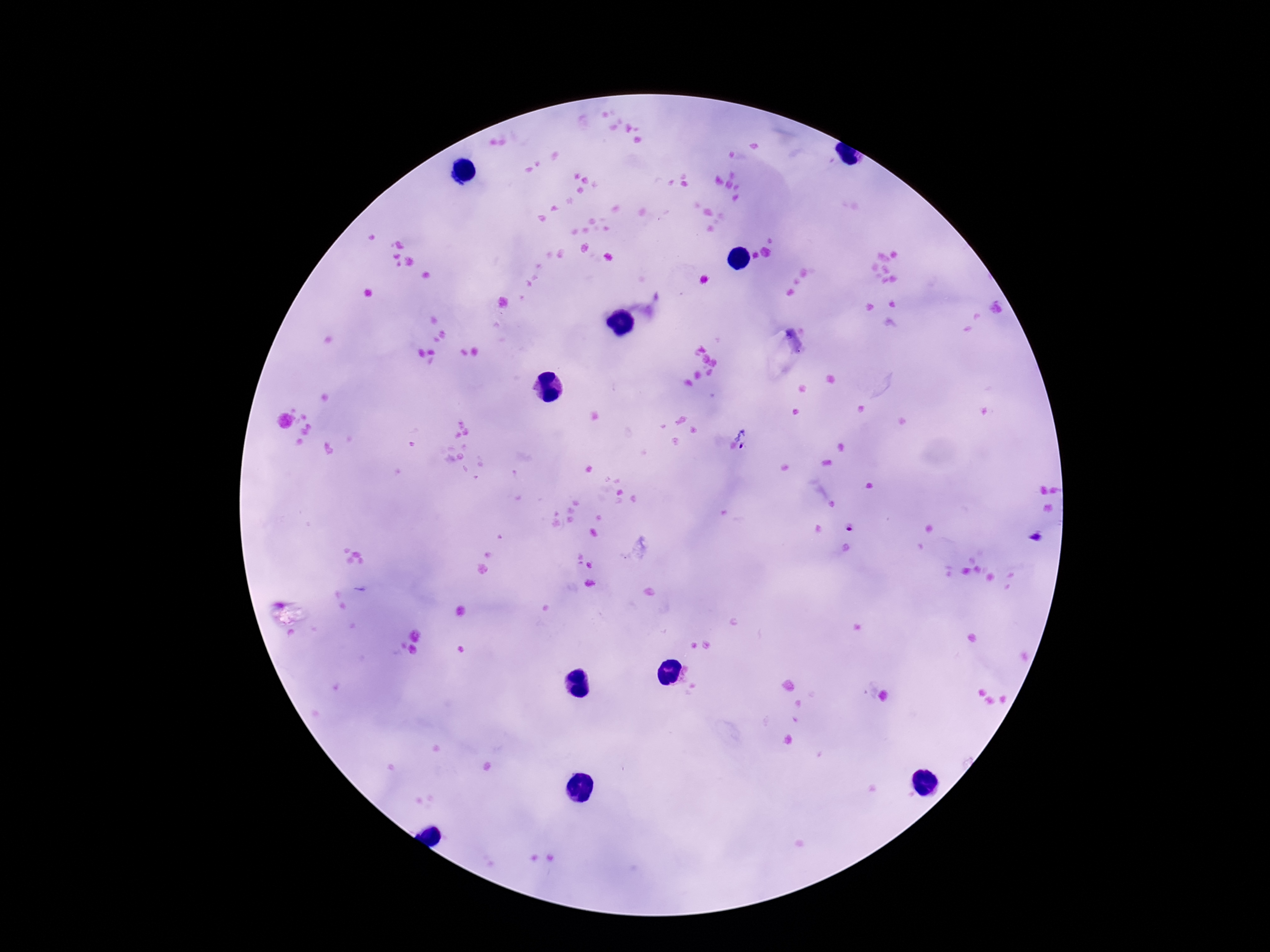

field_of_view: single
capture: smartphone camera through the microscope eyepiece
plasmodium_parasite_locations: 'approximate centers as (x, y) in pixels: (747, 438), (850, 529), (1036, 537)'
stain: Giemsa
patient_malaria_status: positive
image_size: 1270×952 pixels
magnification: 100x
preparation: thick peripheral-blood smear